Name the parasite shown.
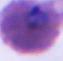

Plasmodium.

modality: micrograph
magnification: 400x or 1000x